Describe the morphology of the red blood cells.
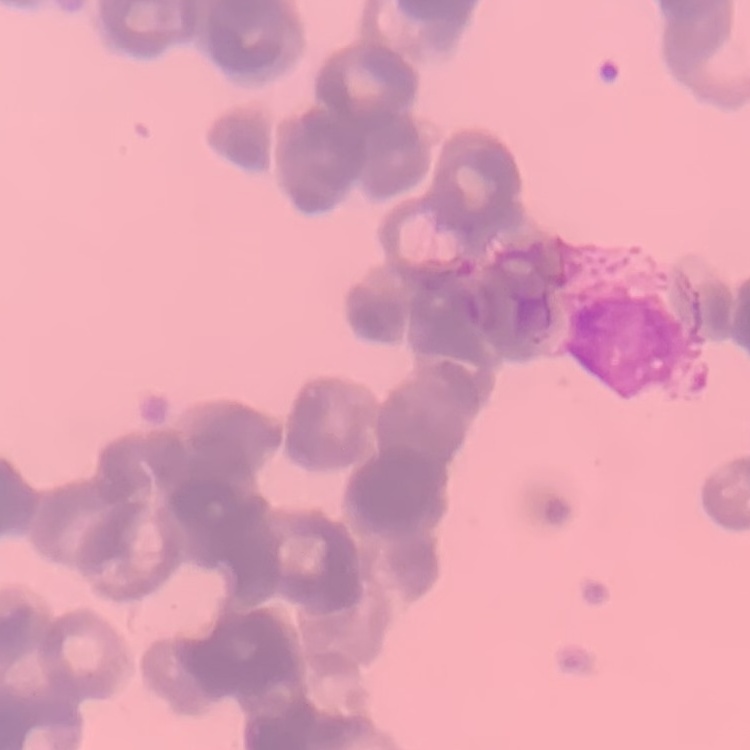

Rouleaux formation.

One tile cut from a larger photomicrograph. Stained with either Field's or Giemsa. Thin blood smear.